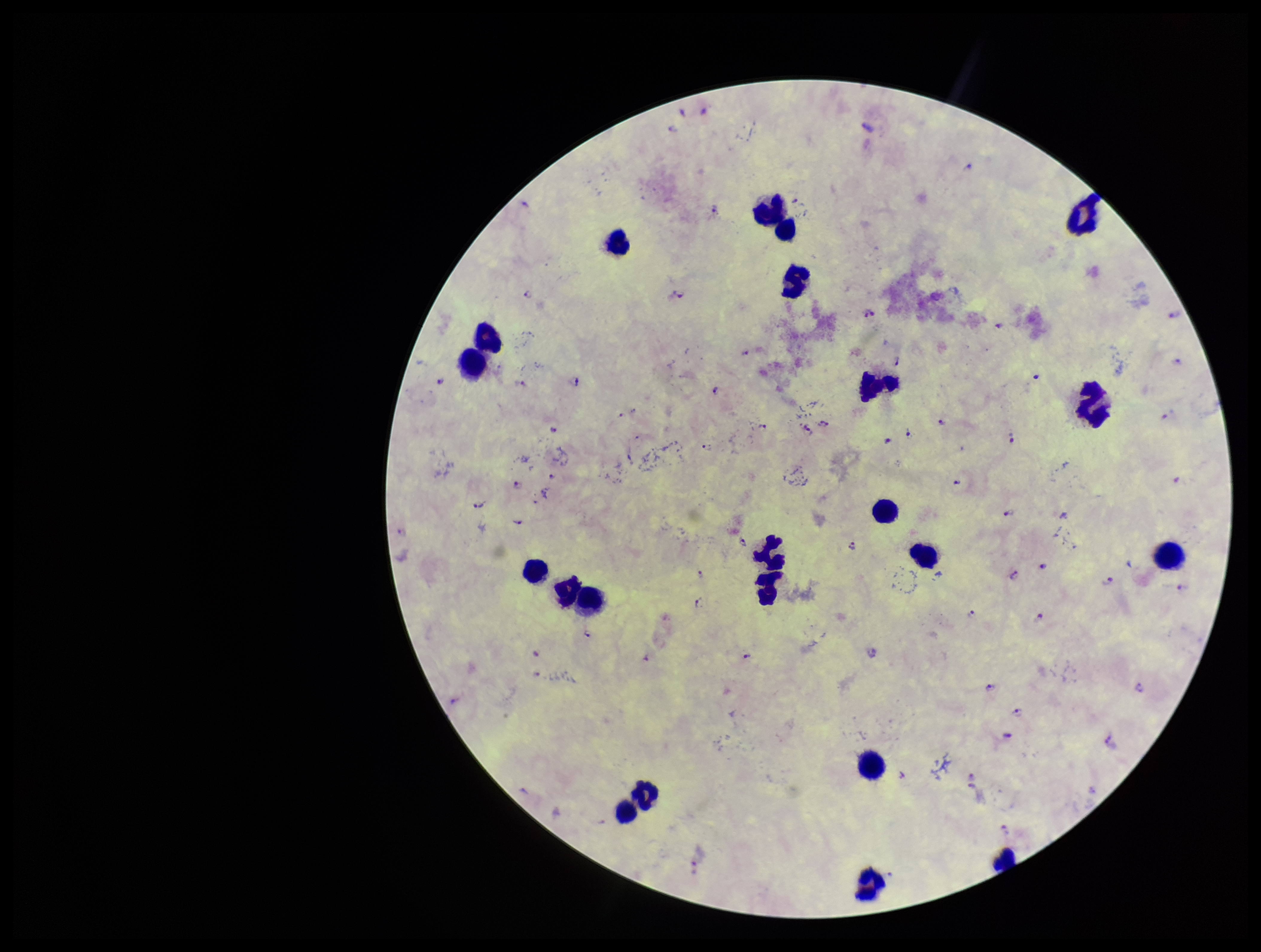
Summary:
  - Parasite count: 52
  - Preparation: thick
  - Plasmodium parasites: seen
  - Patient malaria status: positive
  - Field of view: one from this slide
  - Capture: smartphone photograph through the microscope eyepiece
  - Image size: 1261×952 pixels
  - Species reported for this patient: Plasmodium falciparum
  - Leukocyte count: 21
  - Stain: Giemsa